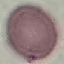
malaria status = uninfected
preparation = thin blood smear
stain = Giemsa
capture = smartphone through the microscope eyepiece
image type = cell patch, automatically extracted from a larger field of view and resized to 64 × 64 pixels